Locate and identify every blood parasite.
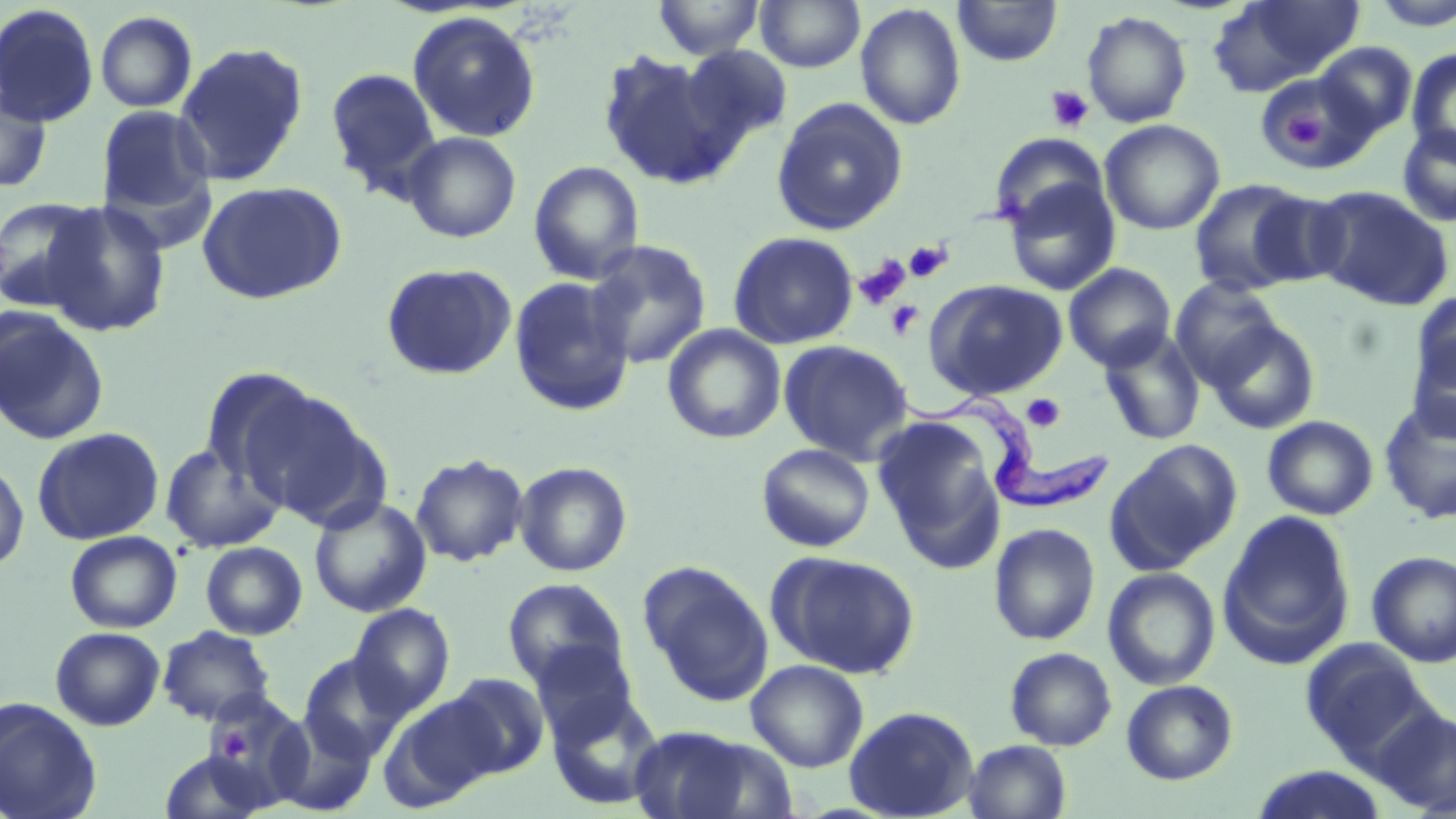
Approximate bounding boxes as named x1/y1/x2/y2 corners in pixels.
Trypanosoma brucei: (x1=893, y1=380, x2=1108, y2=512).
No Plasmodium falciparum, Plasmodium ovale, Plasmodium malariae, Plasmodium vivax, or Babesia divergens observed.

slide-level diagnosis = Trypanosoma brucei
platelet locations = approximate bounding boxes as named x1/y1/x2/y2 corners in pixels: (x1=1045, y1=85, x2=1095, y2=133), (x1=1282, y1=109, x2=1325, y2=153), (x1=904, y1=240, x2=953, y2=283), (x1=854, y1=255, x2=911, y2=310), (x1=885, y1=300, x2=924, y2=340), (x1=1022, y1=394, x2=1066, y2=432), (x1=210, y1=722, x2=253, y2=764)
field of view = single
magnification = 1000x
preparation = thin blood smear
image size = 1456×819 pixels
uninfected red blood cell locations = approximate bounding boxes as named x1/y1/x2/y2 corners in pixels: (x1=653, y1=0, x2=765, y2=59), (x1=755, y1=0, x2=865, y2=72), (x1=1208, y1=0, x2=1364, y2=95), (x1=952, y1=1, x2=1063, y2=67), (x1=1370, y1=1, x2=1456, y2=32), (x1=856, y1=3, x2=967, y2=131), (x1=0, y1=4, x2=100, y2=127), (x1=95, y1=10, x2=198, y2=112), (x1=1082, y1=10, x2=1193, y2=127), (x1=407, y1=11, x2=541, y2=143), (x1=174, y1=41, x2=309, y2=186), (x1=1315, y1=42, x2=1417, y2=138), (x1=681, y1=46, x2=791, y2=149), (x1=1406, y1=47, x2=1456, y2=161), (x1=598, y1=50, x2=737, y2=188), (x1=326, y1=68, x2=441, y2=194), (x1=1257, y1=69, x2=1376, y2=177), (x1=0, y1=84, x2=52, y2=193), (x1=771, y1=97, x2=909, y2=236), (x1=96, y1=105, x2=214, y2=220), (x1=1100, y1=119, x2=1225, y2=235), (x1=1397, y1=124, x2=1456, y2=227), (x1=402, y1=131, x2=521, y2=242), (x1=991, y1=133, x2=1109, y2=231), (x1=528, y1=160, x2=645, y2=285), (x1=1002, y1=176, x2=1121, y2=296), (x1=1188, y1=178, x2=1313, y2=297), (x1=197, y1=181, x2=347, y2=304), (x1=1309, y1=186, x2=1454, y2=311), (x1=1247, y1=189, x2=1352, y2=289), (x1=0, y1=196, x2=105, y2=312), (x1=40, y1=200, x2=172, y2=338), (x1=728, y1=231, x2=859, y2=349), (x1=585, y1=240, x2=712, y2=369), (x1=380, y1=262, x2=516, y2=380), (x1=1063, y1=263, x2=1176, y2=372), (x1=508, y1=276, x2=634, y2=416), (x1=1170, y1=277, x2=1284, y2=386), (x1=924, y1=279, x2=1068, y2=401), (x1=1411, y1=291, x2=1456, y2=394), (x1=0, y1=306, x2=109, y2=444), (x1=1205, y1=319, x2=1321, y2=434), (x1=663, y1=324, x2=786, y2=443), (x1=1098, y1=331, x2=1206, y2=446), (x1=1407, y1=332, x2=1456, y2=442), (x1=778, y1=339, x2=915, y2=465), (x1=198, y1=367, x2=320, y2=485), (x1=238, y1=387, x2=385, y2=526), (x1=1379, y1=399, x2=1456, y2=524), (x1=1262, y1=415, x2=1379, y2=520), (x1=874, y1=418, x2=1007, y2=568), (x1=31, y1=427, x2=164, y2=545), (x1=1106, y1=439, x2=1243, y2=574), (x1=756, y1=442, x2=875, y2=552), (x1=160, y1=443, x2=284, y2=553), (x1=410, y1=454, x2=529, y2=566), (x1=0, y1=457, x2=30, y2=573), (x1=514, y1=461, x2=632, y2=577), (x1=308, y1=496, x2=432, y2=617), (x1=1218, y1=512, x2=1356, y2=667), (x1=988, y1=522, x2=1101, y2=646), (x1=65, y1=530, x2=182, y2=633), (x1=200, y1=541, x2=307, y2=639), (x1=1366, y1=550, x2=1456, y2=668), (x1=767, y1=551, x2=921, y2=679), (x1=640, y1=562, x2=774, y2=705), (x1=1102, y1=567, x2=1221, y2=690), (x1=502, y1=578, x2=629, y2=690), (x1=349, y1=604, x2=454, y2=717), (x1=157, y1=625, x2=276, y2=726), (x1=50, y1=626, x2=165, y2=730), (x1=1299, y1=639, x2=1432, y2=766), (x1=530, y1=640, x2=639, y2=743), (x1=1004, y1=646, x2=1117, y2=750), (x1=300, y1=654, x2=407, y2=761), (x1=745, y1=659, x2=869, y2=772), (x1=441, y1=673, x2=550, y2=780), (x1=1121, y1=679, x2=1239, y2=785), (x1=546, y1=691, x2=665, y2=809), (x1=381, y1=694, x2=501, y2=808), (x1=0, y1=696, x2=103, y2=819), (x1=196, y1=696, x2=298, y2=801), (x1=843, y1=705, x2=980, y2=819), (x1=1372, y1=706, x2=1456, y2=816), (x1=268, y1=713, x2=377, y2=816), (x1=627, y1=725, x2=786, y2=819), (x1=962, y1=739, x2=1073, y2=819), (x1=157, y1=747, x2=276, y2=819), (x1=1250, y1=766, x2=1389, y2=819)
modality = optical microscopy
stain = May-Grünwald-Giemsa